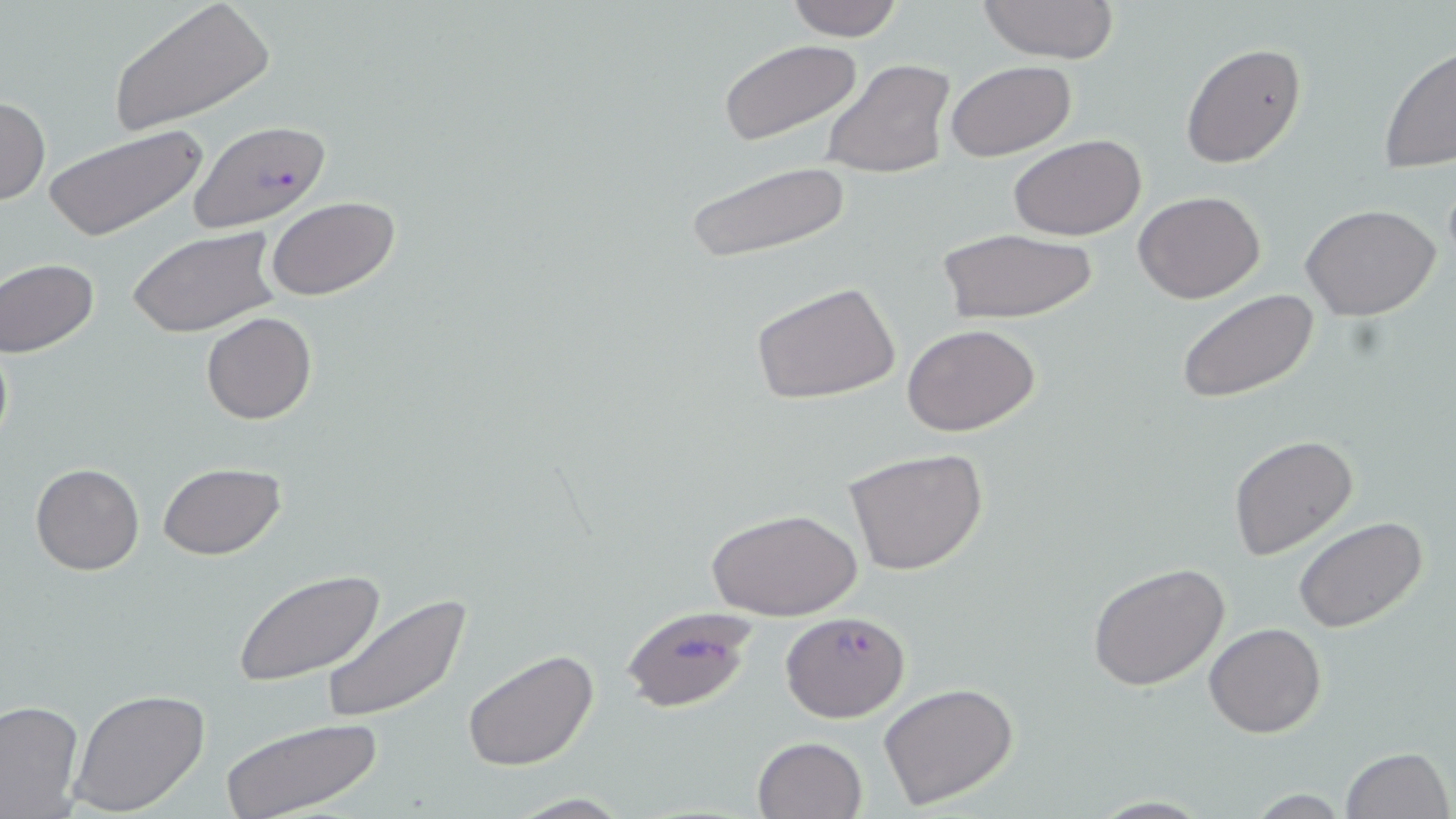
Summary:
  - Coordinate format: approximate bounding boxes as (x1,y1)-(x2,y2) corner pairs in pixels
  - Uninfected red blood cell locations: (782,0)-(910,42), (975,0)-(1121,65), (106,1)-(274,136), (718,38)-(862,147), (1180,42)-(1307,168), (1378,46)-(1456,174), (821,58)-(956,179), (945,60)-(1075,162), (0,95)-(50,206), (44,124)-(209,242), (1009,134)-(1147,240), (684,159)-(855,264), (1133,190)-(1266,304), (266,196)-(402,301), (1301,203)-(1443,320), (128,226)-(280,338), (935,226)-(1102,326), (1,258)-(100,359), (751,280)-(902,407), (1174,287)-(1320,404), (201,312)-(317,425), (902,323)-(1040,437), (1228,434)-(1359,560), (844,447)-(989,578), (30,462)-(144,575), (159,463)-(286,560), (707,507)-(860,622), (1293,518)-(1427,634), (1087,562)-(1230,691), (233,571)-(386,687), (319,594)-(474,724), (1205,621)-(1326,737), (461,647)-(601,772), (879,681)-(1021,810), (68,687)-(211,817), (0,698)-(84,816), (218,717)-(386,819), (752,735)-(869,819), (1340,746)-(1452,819), (506,793)-(637,817), (1088,796)-(1217,818)
  - Plasmodium falciparum-infected red blood cell locations: (189,120)-(332,231), (618,604)-(760,714), (781,610)-(910,721)
  - Slide-level diagnosis: Plasmodium falciparum
  - Stain: May-Grünwald-Giemsa
  - Image size: 1456×819 pixels
  - Magnification: 1000x
  - Modality: light microscopy
  - Preparation: thin blood film
  - Field of view: one of a larger specimen